Give the position of every Plasmodium parasite.
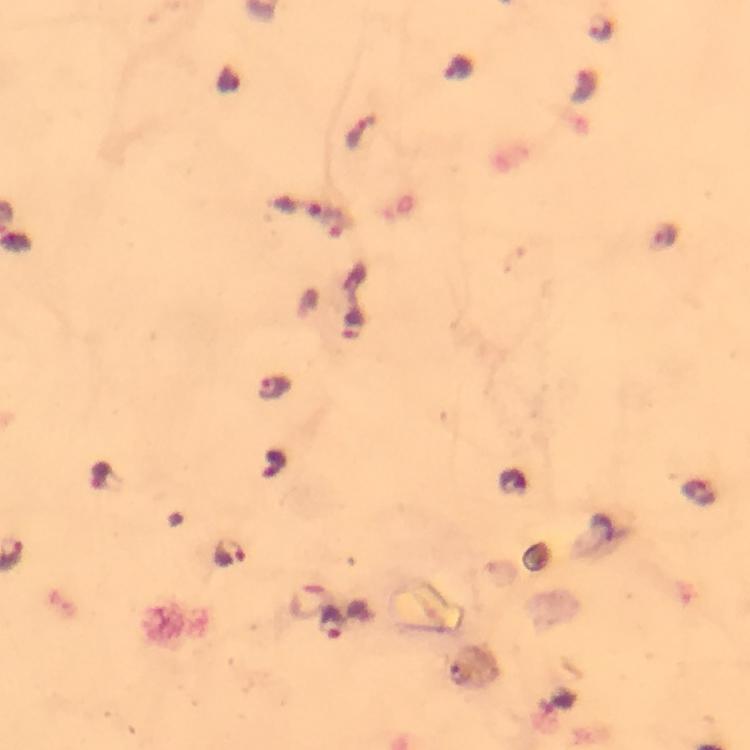

Approximate object centers, in pixels from the top-left corner.
Plasmodium parasites: (x=600, y=28), (x=458, y=68), (x=357, y=132), (x=662, y=235), (x=275, y=389), (x=230, y=553), (x=332, y=623).

preparation = thick blood film
magnification = 100x
image size = 750×750 pixels
context = from a malaria diagnostic workup
immersion oil = used
stain = Giemsa
cropped from = one field of view
capture = smartphone camera through the microscope